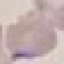
Summary:
  - Malaria status: uninfected
  - Capture: smartphone through the microscope eyepiece
  - Image type: automatically extracted cell patch, resized to 64 × 64 pixels
  - Stain: Giemsa
  - Preparation: thin blood smear